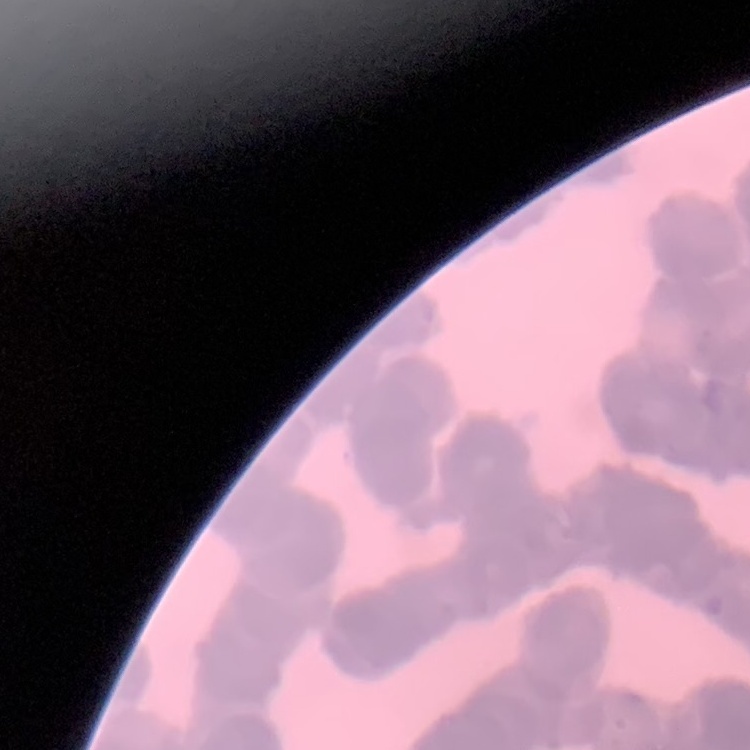
red blood cell morphology = rouleaux formation
preparation = thin peripheral smear
image type = one tile cut from a larger photomicrograph
stain = Field's or Giemsa